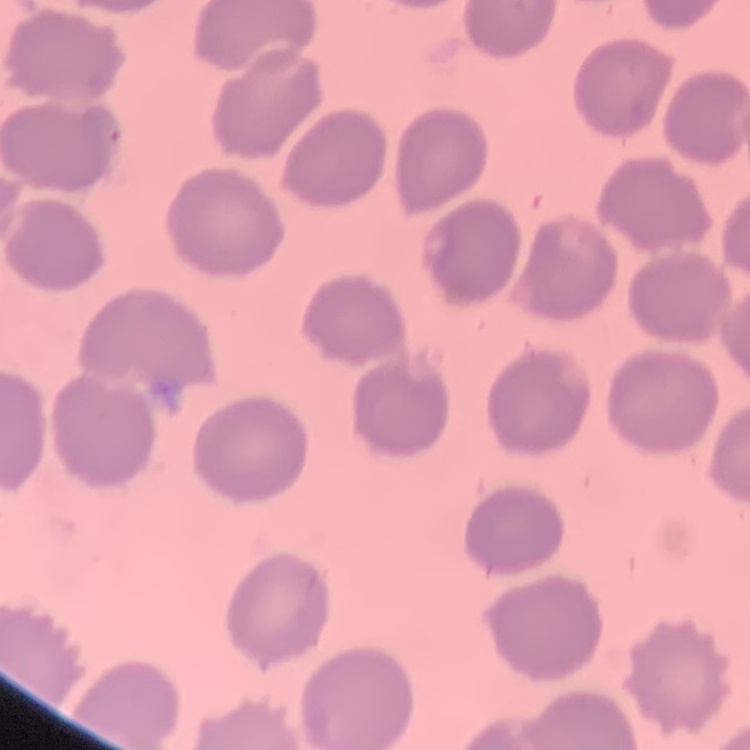
The erythrocytes show no rouleaux formation. One tile cut from a larger photomicrograph. Stained with either Field's or Giemsa. Thin blood smear.